Describe the morphology of the erythrocytes.
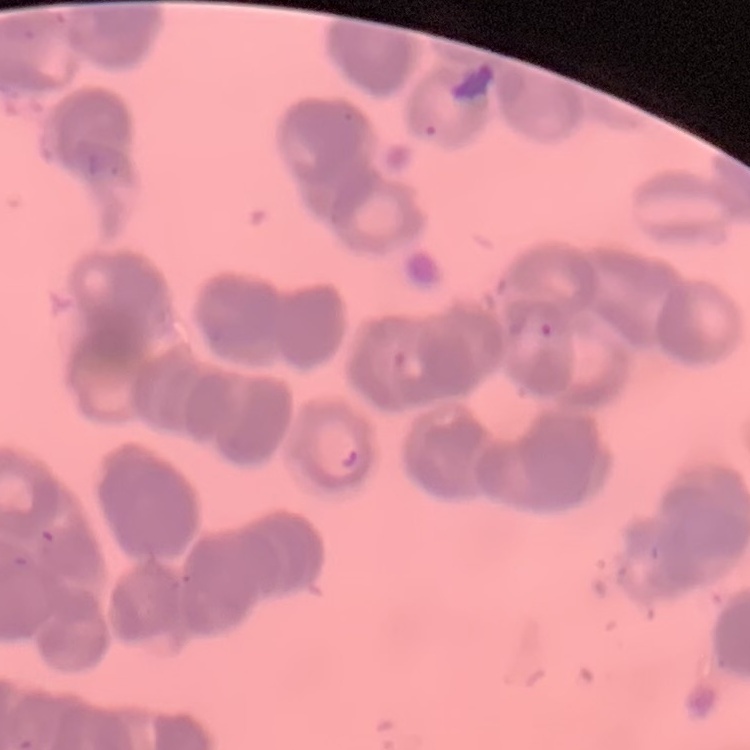
Rouleaux formation.

Thin blood film. Square crop of a larger photomicrograph. Stained with either Field's or Giemsa.